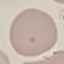

{
  "malaria_status": "uninfected",
  "stain": "Giemsa",
  "preparation": "thin blood smear",
  "capture": "smartphone through the microscope eyepiece",
  "image_type": "automatically extracted cell patch, resized to 64 × 64 pixels"
}